Assess this cell for malaria.
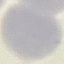
It is uninfected.

Summary:
  - Image type: automatically extracted cell patch, resized to 64 × 64 pixels
  - Stain: Giemsa
  - Preparation: thin blood film
  - Capture: smartphone through the microscope eyepiece